Report the malaria status of this cell.
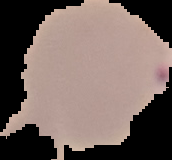

It is parasitized.

{
  "preparation": "thin blood smear",
  "image_size": "172×160 pixels",
  "image_type": "cell region segmented out of the field of view; surrounding area masked to black"
}